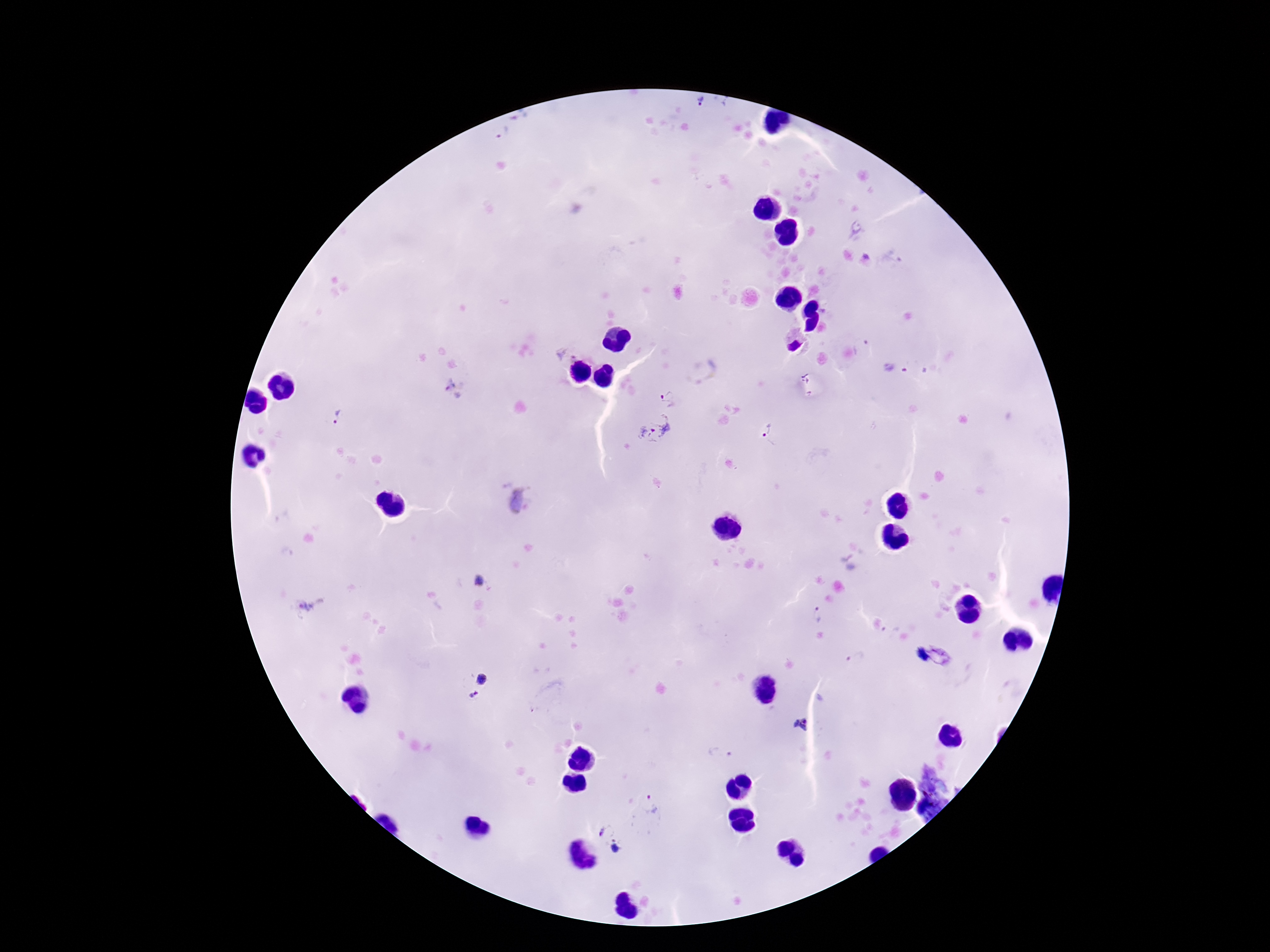 Approximate object centers, in pixels from the top-left corner. Plasmodium parasite locations: (x=701, y=103), (x=504, y=133), (x=454, y=389), (x=670, y=395), (x=335, y=417), (x=657, y=427), (x=768, y=435), (x=481, y=582), (x=820, y=615), (x=483, y=677), (x=475, y=695), (x=802, y=724), (x=651, y=805), (x=610, y=838). One field from this slide. Giemsa stain. 100x magnification. Image is 1270×952 pixels. Smartphone photograph taken through the microscope eyepiece. Patient malaria status: infected. Thick peripheral-blood smear.